Give the preparation type.
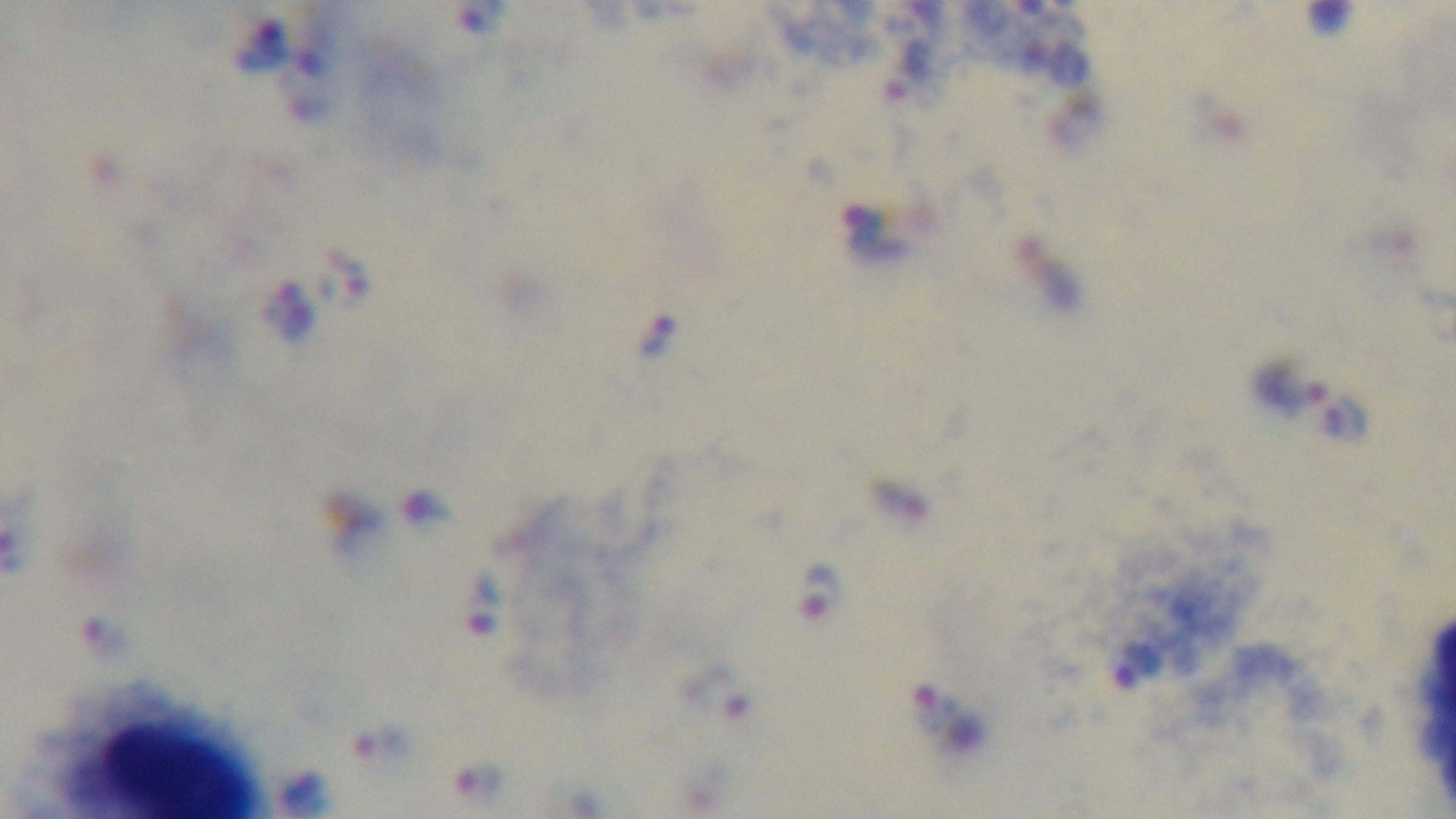

Thick.

capture: mounted 4K digital camera
malaria_status: positive
field_of_view: one from the slide
modality: light microscopy
objective: 100x oil immersion
stain: Giemsa